Identify the blood parasite species.
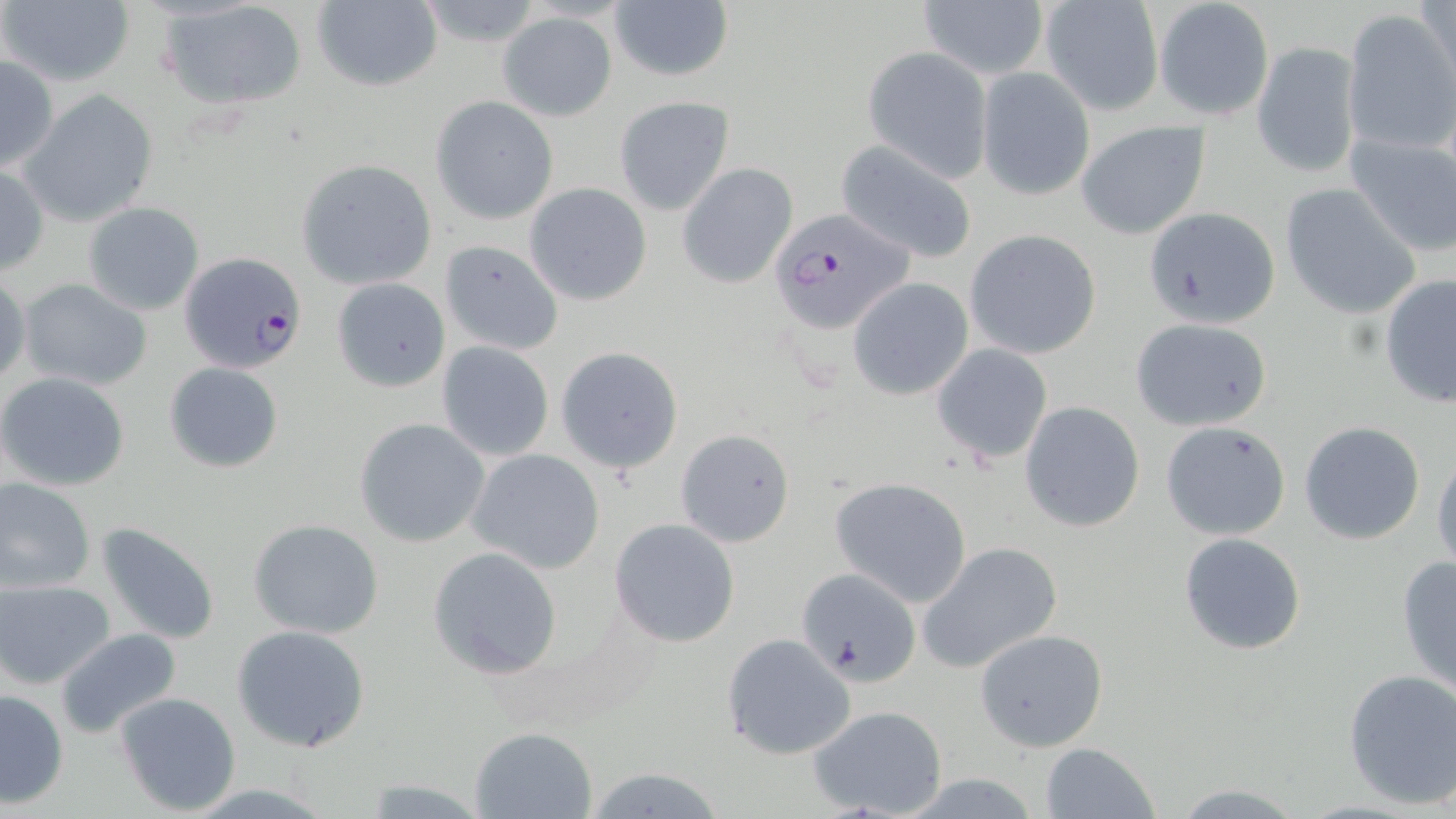

Plasmodium falciparum.

Approximate bounding boxes as [x1, y1, x2, y2] in pixels. Plasmodium falciparum-infected red blood cell locations: [767, 207, 916, 336], [179, 253, 309, 377]. Uninfected red blood cell locations: [2, 0, 135, 88], [310, 0, 443, 91], [416, 0, 548, 51], [1418, 0, 1455, 92], [160, 1, 309, 112], [918, 1, 1048, 81], [1154, 1, 1273, 121], [609, 2, 734, 84], [1038, 2, 1162, 116], [1342, 8, 1454, 155], [498, 12, 617, 121], [1252, 40, 1362, 177], [863, 47, 992, 180], [0, 54, 59, 173], [977, 68, 1095, 201], [19, 89, 159, 229], [431, 94, 559, 226], [614, 96, 734, 215], [1076, 120, 1211, 239], [1344, 132, 1456, 257], [834, 139, 979, 265], [296, 159, 438, 289], [677, 162, 798, 288], [0, 163, 48, 275], [524, 183, 652, 306], [1280, 184, 1422, 320], [82, 201, 204, 316], [1141, 206, 1281, 329], [964, 229, 1101, 360], [439, 239, 564, 356], [0, 271, 30, 386], [330, 276, 451, 393], [1378, 276, 1456, 408], [18, 278, 153, 392], [848, 278, 975, 400], [1129, 317, 1273, 429], [436, 341, 556, 462], [932, 343, 1053, 465], [555, 344, 685, 473], [163, 361, 285, 474], [0, 372, 131, 492], [1020, 401, 1146, 534], [354, 418, 490, 547], [1159, 420, 1292, 540], [1299, 420, 1425, 544], [675, 429, 796, 548], [467, 449, 605, 574], [1431, 450, 1456, 570], [0, 478, 97, 595], [830, 478, 971, 607], [247, 518, 384, 640], [609, 518, 740, 648], [97, 521, 222, 647], [1177, 531, 1308, 656], [916, 541, 1063, 674], [428, 546, 561, 680], [1394, 554, 1456, 699], [796, 569, 922, 686], [1, 580, 116, 688], [231, 624, 372, 753], [975, 628, 1108, 752], [56, 629, 182, 742], [720, 634, 857, 761], [1342, 667, 1456, 809], [0, 689, 69, 809], [113, 691, 242, 815], [807, 704, 947, 818], [469, 727, 596, 818], [1040, 742, 1160, 819], [579, 765, 732, 819], [896, 774, 1045, 817], [358, 778, 492, 816], [1165, 782, 1314, 818]. Light microscopy. 1000x magnification. Thin blood film. Image is 1456×819 pixels. Single field of view. May-Grünwald-Giemsa-stained preparation.